Classify this cell by malaria status.
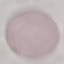

It is uninfected.

capture: smartphone through the microscope eyepiece
preparation: thin blood film
image_type: cell patch, automatically extracted from a larger field of view and resized to 64 × 64 pixels
stain: Giemsa